Describe the morphology of the erythrocytes.
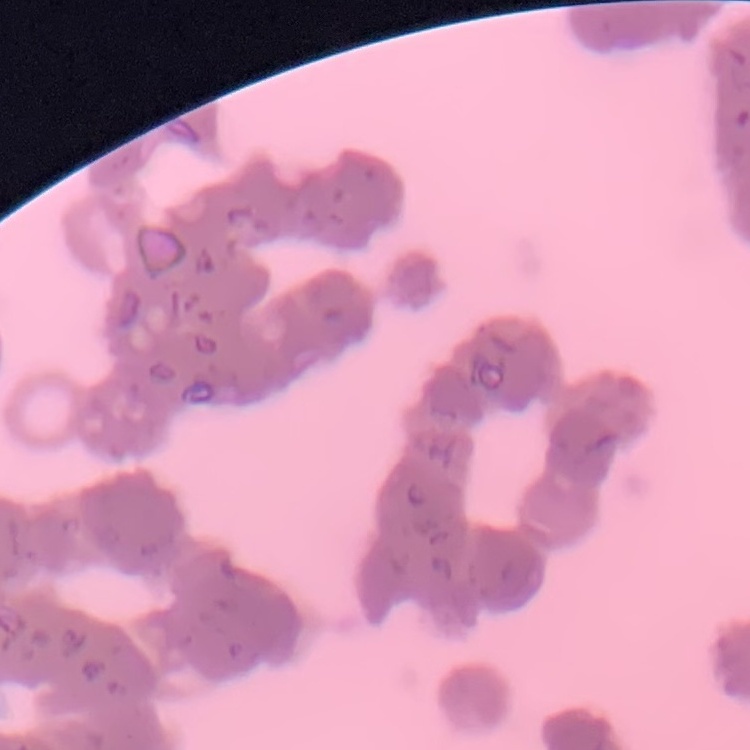

Rouleaux formation.

{
  "image_type": "one tile cut from a larger photomicrograph",
  "preparation": "thin blood film",
  "stain": "Field's or Giemsa"
}